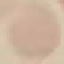
Summary:
  - Malaria status: uninfected
  - Capture: smartphone through the microscope eyepiece
  - Stain: Giemsa
  - Image type: cell patch, automatically extracted from a larger field of view and resized to 64 × 64 pixels
  - Preparation: thin blood smear